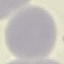

Result: no malaria parasites detected. Automatically extracted cell patch, resized to 64 × 64 pixels. Acquired by smartphone through the microscope eyepiece. Thin blood film. Giemsa-stained preparation.